Assess this cell for malaria.
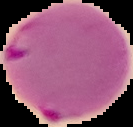
Parasitized.

{
  "image_type": "segmented cell region with the area outside set to black",
  "preparation": "thin blood film",
  "image_size": "133×127 pixels"
}